Assess this cell for malaria.
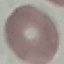

It is uninfected.

Summary:
  - Preparation: thin blood smear
  - Capture: smartphone through the microscope eyepiece
  - Image type: cell patch, automatically extracted from a larger field of view and resized to 64 × 64 pixels
  - Stain: Giemsa